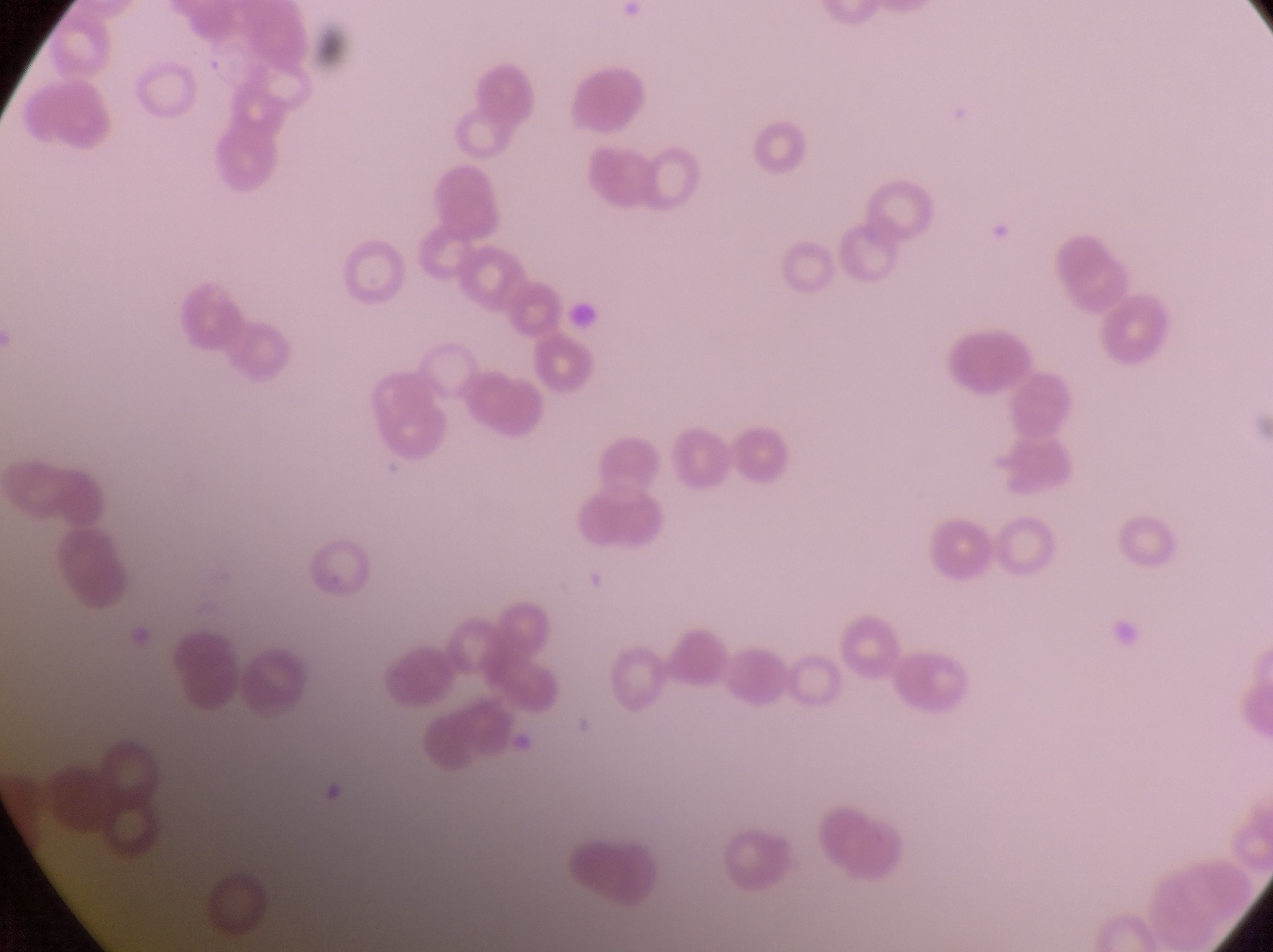 Approximate bounding boxes as left top right bottom in pixels. Artifact (platelet-like body, stain precipitate, or debris) locations: 561 299 603 341. At a magnification of 1000x. Image is 1273×952 pixels. Thin blood smear. One field of view. Sample from Uganda. Captured by a smartphone held over the eyepiece of an Olympus CX-23 microscope.